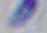
Micrograph. 1000x magnification. Toxoplasma gondii is seen.